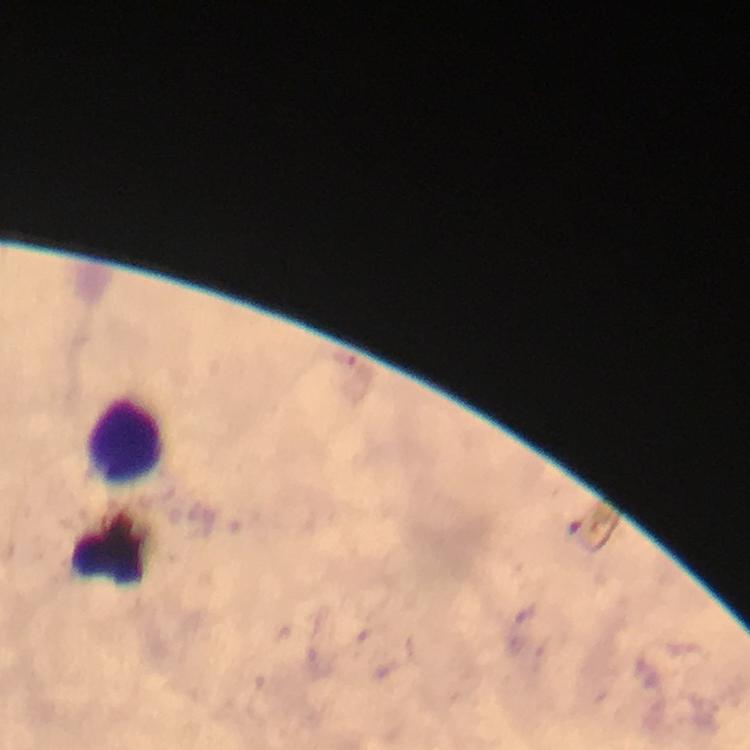
preparation: thick blood smear
immersion_oil: applied
leukocyte_locations: 'approximate centers as [x, y] in pixels: [127, 439]'
context: from a malaria diagnostic workup
capture: smartphone mounted on the microscope
cropped_from: a single field of view
stain: Giemsa
image_size: 750×750 pixels
plasmodium_parasites: none seen
magnification: 100x